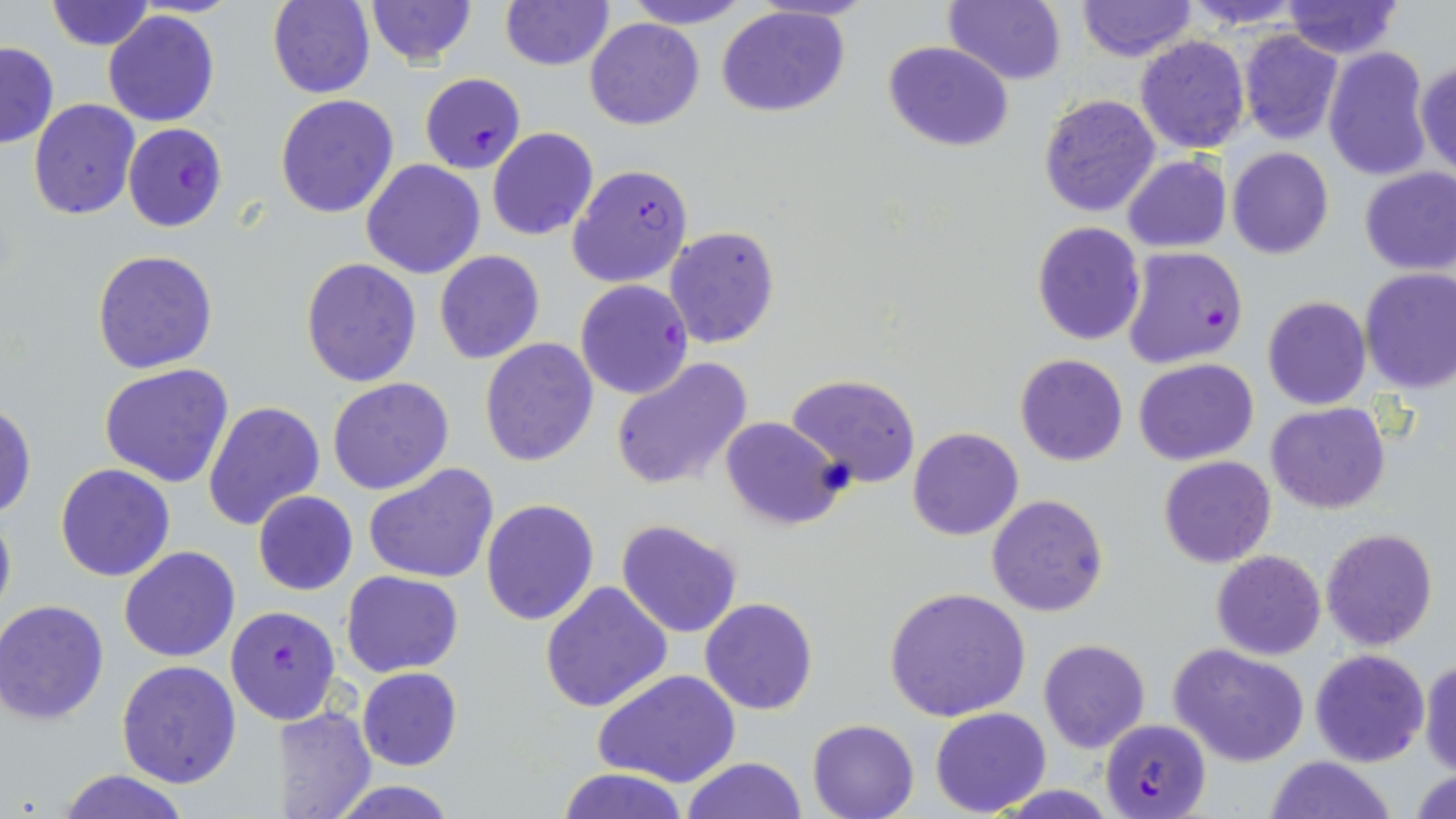

slide-level diagnosis = Plasmodium falciparum
image size = 1456×819 pixels
stain = May-Grünwald-Giemsa
uninfected red blood cell locations = approximate bounding boxes as [x1, y1, x2, y2] in pixels: [366, 0, 475, 66], [621, 0, 752, 28], [945, 0, 1066, 85], [1075, 0, 1199, 63], [1182, 0, 1308, 30], [43, 1, 156, 51], [268, 1, 375, 99], [500, 1, 615, 71], [1279, 1, 1403, 59], [716, 5, 849, 118], [104, 10, 219, 126], [584, 17, 704, 130], [1238, 31, 1344, 144], [1136, 35, 1250, 154], [1, 41, 58, 149], [883, 41, 1014, 152], [1322, 46, 1433, 181], [1415, 59, 1455, 179], [1038, 93, 1160, 218], [275, 94, 399, 218], [29, 98, 140, 219], [486, 128, 598, 242], [1226, 147, 1333, 260], [1123, 154, 1231, 253], [361, 158, 486, 278], [1358, 168, 1455, 276], [1031, 221, 1146, 346], [664, 225, 781, 349], [91, 249, 218, 374], [434, 251, 544, 364], [300, 256, 422, 388], [1358, 267, 1456, 392], [1262, 296, 1370, 410], [478, 338, 599, 466], [1015, 353, 1127, 466], [610, 357, 752, 491], [1134, 357, 1259, 465], [99, 363, 234, 487], [787, 373, 921, 487], [327, 377, 454, 495], [1, 401, 36, 519], [203, 401, 326, 534], [1267, 402, 1389, 514], [720, 416, 844, 529], [908, 426, 1023, 541], [1158, 455, 1275, 568], [363, 463, 499, 584], [55, 465, 175, 583], [253, 491, 358, 594], [986, 493, 1109, 617], [480, 499, 599, 625], [0, 504, 16, 633], [615, 519, 743, 638], [1319, 526, 1438, 650], [118, 546, 240, 663], [1210, 550, 1327, 660], [340, 570, 465, 677], [539, 582, 673, 715], [886, 587, 1029, 723], [701, 597, 817, 715], [0, 601, 109, 724], [1038, 639, 1151, 754], [1169, 642, 1310, 766], [1309, 648, 1431, 767], [1418, 657, 1456, 776], [115, 659, 242, 789], [356, 666, 461, 770], [595, 671, 740, 788], [277, 706, 377, 819], [931, 707, 1052, 815], [806, 718, 919, 819], [1267, 754, 1397, 819], [681, 756, 805, 819], [556, 767, 690, 819], [1410, 768, 1456, 819], [56, 769, 192, 819], [326, 778, 459, 817]
preparation = thin blood smear
magnification = 1000x
field of view = one of a larger specimen
Plasmodium falciparum-infected red blood cell locations = approximate bounding boxes as [x1, y1, x2, y2] in pixels: [419, 73, 526, 174], [122, 122, 228, 232], [567, 164, 694, 287], [1122, 246, 1248, 370], [575, 279, 693, 399], [226, 605, 342, 724], [1101, 720, 1212, 817]
modality = optical microscopy